Outline each Plasmodium falciparum-infected red blood cell.
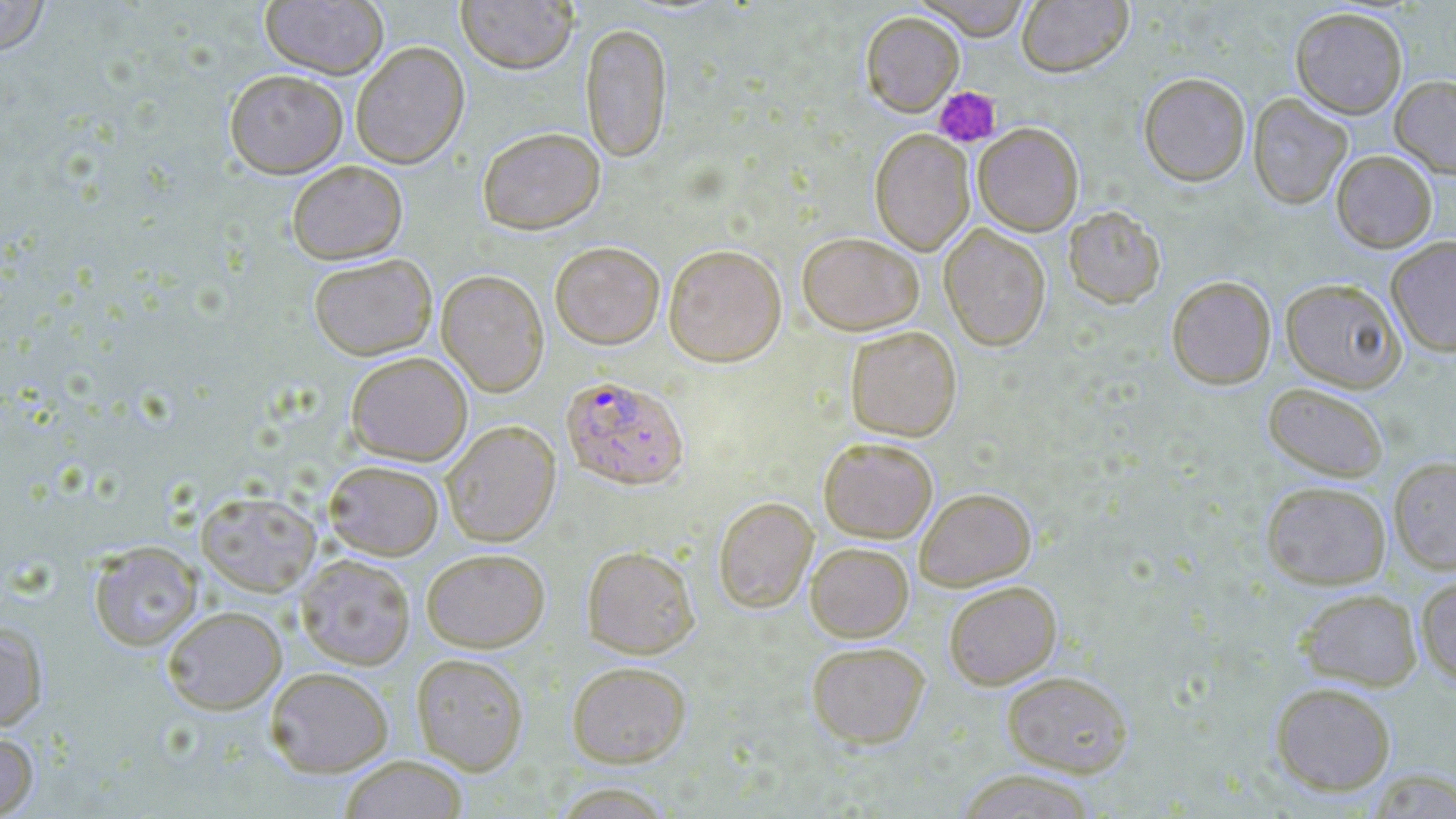

Approximate bounding boxes as [x1, y1, x2, y2] in pixels.
Plasmodium falciparum-infected red blood cells: [561, 375, 689, 489].

Summary:
  - Platelet locations: [934, 87, 1001, 147]
  - Uninfected red blood cell locations: [0, 0, 51, 56], [260, 0, 389, 78], [456, 0, 578, 74], [914, 0, 1032, 40], [1016, 1, 1132, 76], [1291, 6, 1407, 118], [860, 11, 964, 116], [580, 22, 673, 162], [350, 41, 470, 168], [224, 69, 348, 178], [1138, 72, 1250, 186], [1390, 75, 1456, 179], [1248, 93, 1352, 209], [973, 122, 1084, 236], [477, 126, 605, 234], [870, 129, 975, 255], [1331, 150, 1437, 252], [287, 160, 408, 264], [1063, 205, 1166, 309], [939, 223, 1051, 351], [797, 231, 924, 334], [1386, 235, 1456, 357], [550, 241, 665, 349], [663, 243, 786, 366], [308, 253, 437, 360], [436, 269, 549, 396], [1167, 276, 1276, 389], [1281, 277, 1405, 392], [845, 325, 962, 441], [346, 351, 473, 466], [1263, 382, 1388, 482], [441, 420, 561, 546], [819, 436, 938, 542], [1389, 455, 1456, 575], [324, 459, 444, 560], [1261, 480, 1391, 589], [915, 487, 1036, 590], [196, 490, 321, 596], [713, 496, 818, 612], [88, 540, 203, 651], [805, 542, 913, 641], [582, 545, 699, 658], [421, 547, 550, 652], [296, 553, 416, 670], [1415, 573, 1456, 689], [944, 580, 1061, 689], [1296, 588, 1423, 691], [162, 605, 286, 714], [0, 620, 48, 731], [806, 641, 931, 749], [410, 652, 529, 774], [567, 660, 691, 767], [265, 666, 393, 777], [1001, 669, 1133, 776], [1270, 681, 1396, 796], [0, 730, 39, 817], [338, 755, 469, 818], [953, 769, 1101, 818]
  - Slide-level diagnosis: Plasmodium falciparum
  - Image size: 1456×819 pixels
  - Magnification: 1000x
  - Field of view: one of a larger specimen
  - Preparation: thin blood film
  - Modality: light microscopy
  - Stain: May-Grünwald-Giemsa